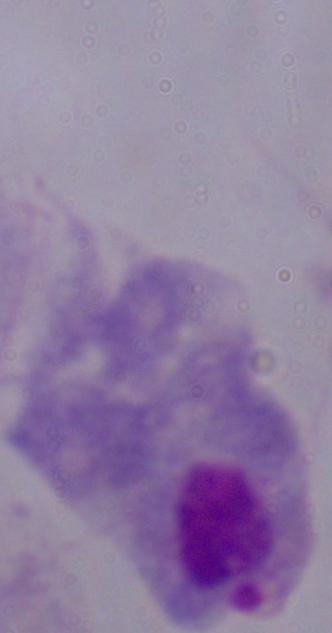

Summary:
  - Modality: micrograph
  - Identification: trichomonad
  - Magnification: 1000x